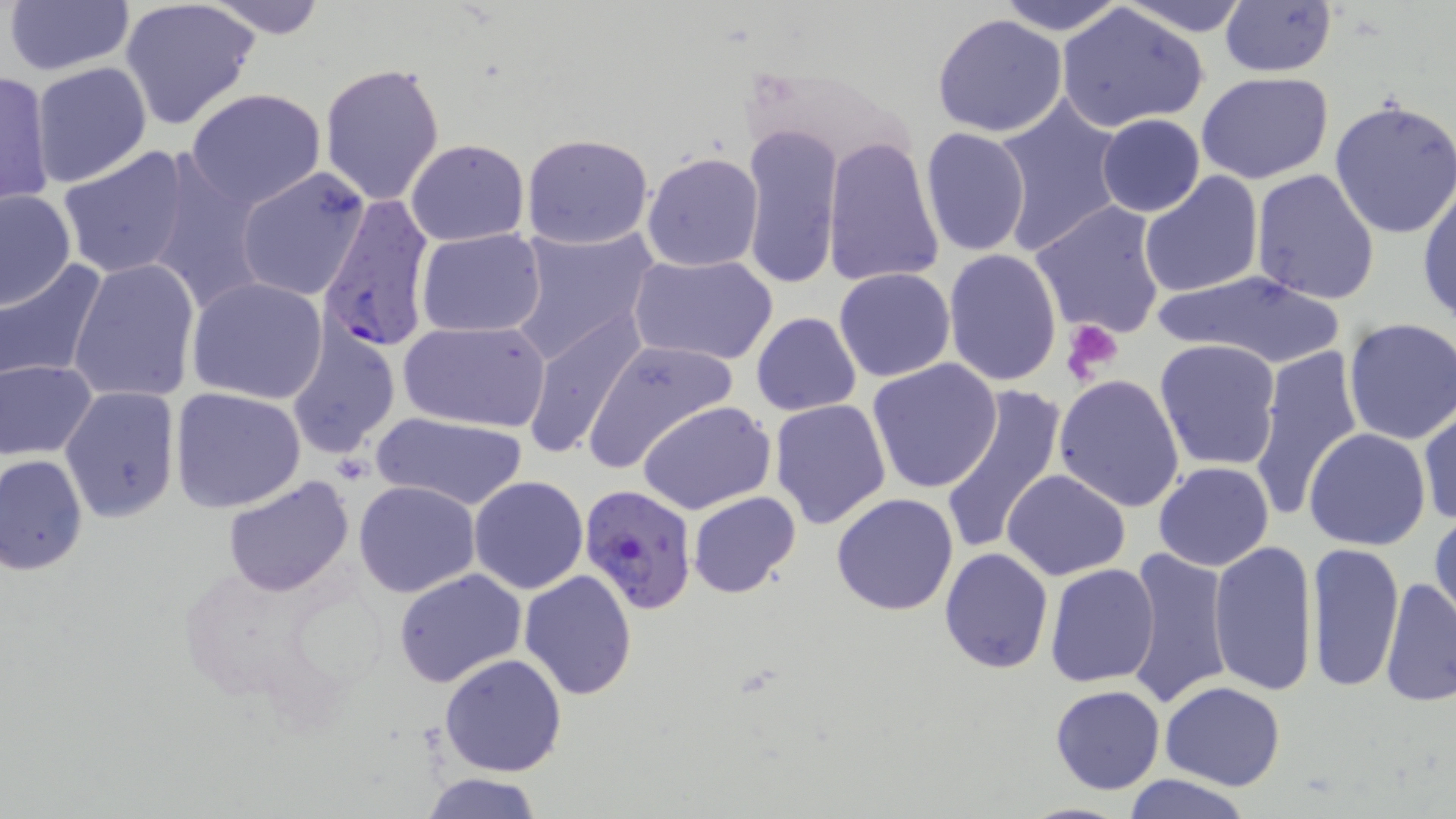
Approximate bounding boxes as (x1, y1, x2, y2) in pixels. Platelet locations: (1062, 320, 1123, 386). Plasmodium falciparum-infected red blood cell locations: (317, 193, 436, 355), (576, 484, 698, 615). Uninfected red blood cell locations: (3, 0, 135, 76), (199, 0, 331, 38), (991, 0, 1129, 35), (1117, 0, 1253, 37), (118, 1, 261, 131), (1219, 1, 1338, 77), (1056, 3, 1209, 132), (932, 13, 1069, 137), (30, 61, 155, 188), (319, 61, 445, 206), (0, 69, 56, 209), (1195, 72, 1334, 183), (185, 88, 326, 210), (990, 94, 1127, 256), (1329, 96, 1456, 240), (1096, 114, 1205, 218), (740, 123, 843, 290), (920, 126, 1032, 258), (520, 133, 654, 249), (822, 136, 945, 287), (405, 139, 530, 245), (57, 145, 194, 280), (641, 151, 764, 272), (149, 162, 269, 316), (236, 166, 371, 302), (1250, 167, 1382, 304), (1137, 171, 1265, 298), (1416, 183, 1456, 327), (1, 189, 76, 311), (1029, 201, 1168, 341), (507, 223, 660, 367), (416, 229, 547, 336), (943, 249, 1062, 387), (627, 252, 778, 367), (68, 256, 203, 403), (0, 259, 108, 385), (833, 267, 957, 383), (1157, 271, 1350, 369), (187, 277, 329, 405), (520, 308, 649, 462), (751, 313, 861, 416), (1339, 317, 1456, 446), (397, 318, 551, 432), (287, 326, 402, 460), (1153, 338, 1283, 470), (582, 339, 735, 471), (1246, 343, 1364, 520), (0, 358, 98, 461), (867, 359, 1002, 492), (1053, 373, 1185, 512), (60, 384, 181, 522), (941, 385, 1066, 558), (169, 386, 306, 513), (769, 399, 893, 529), (639, 401, 775, 515), (1418, 405, 1455, 528), (372, 412, 528, 511), (1304, 427, 1433, 550), (1, 453, 89, 574), (1152, 461, 1274, 570), (1003, 469, 1131, 581), (469, 475, 589, 595), (221, 476, 354, 597), (354, 480, 481, 598), (687, 491, 801, 598), (830, 492, 959, 615), (1429, 507, 1455, 632), (1207, 539, 1318, 696), (1303, 540, 1404, 692), (939, 547, 1054, 674), (1128, 547, 1234, 709), (1044, 562, 1161, 686), (393, 567, 527, 687), (519, 569, 636, 701), (1380, 575, 1456, 707), (439, 653, 568, 775), (1159, 680, 1285, 790), (1050, 684, 1164, 794), (422, 773, 543, 819), (1119, 773, 1254, 818), (1011, 801, 1145, 819). Slide-level diagnosis: Plasmodium falciparum. Image is 1456×819 pixels. 1000x magnification. May-Grünwald-Giemsa stain. Thin blood film. Single field of view. Optical microscopy.